Classify this cell by malaria status.
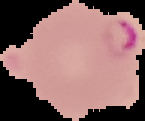
It is parasitized.

Summary:
  - Preparation: thin blood film
  - Image type: segmented cell region with the area outside set to black
  - Image size: 145×121 pixels